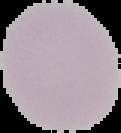

image_type: segmented cell region on a black background
image_size: 121×133 pixels
malaria_status: uninfected
preparation: thin blood film